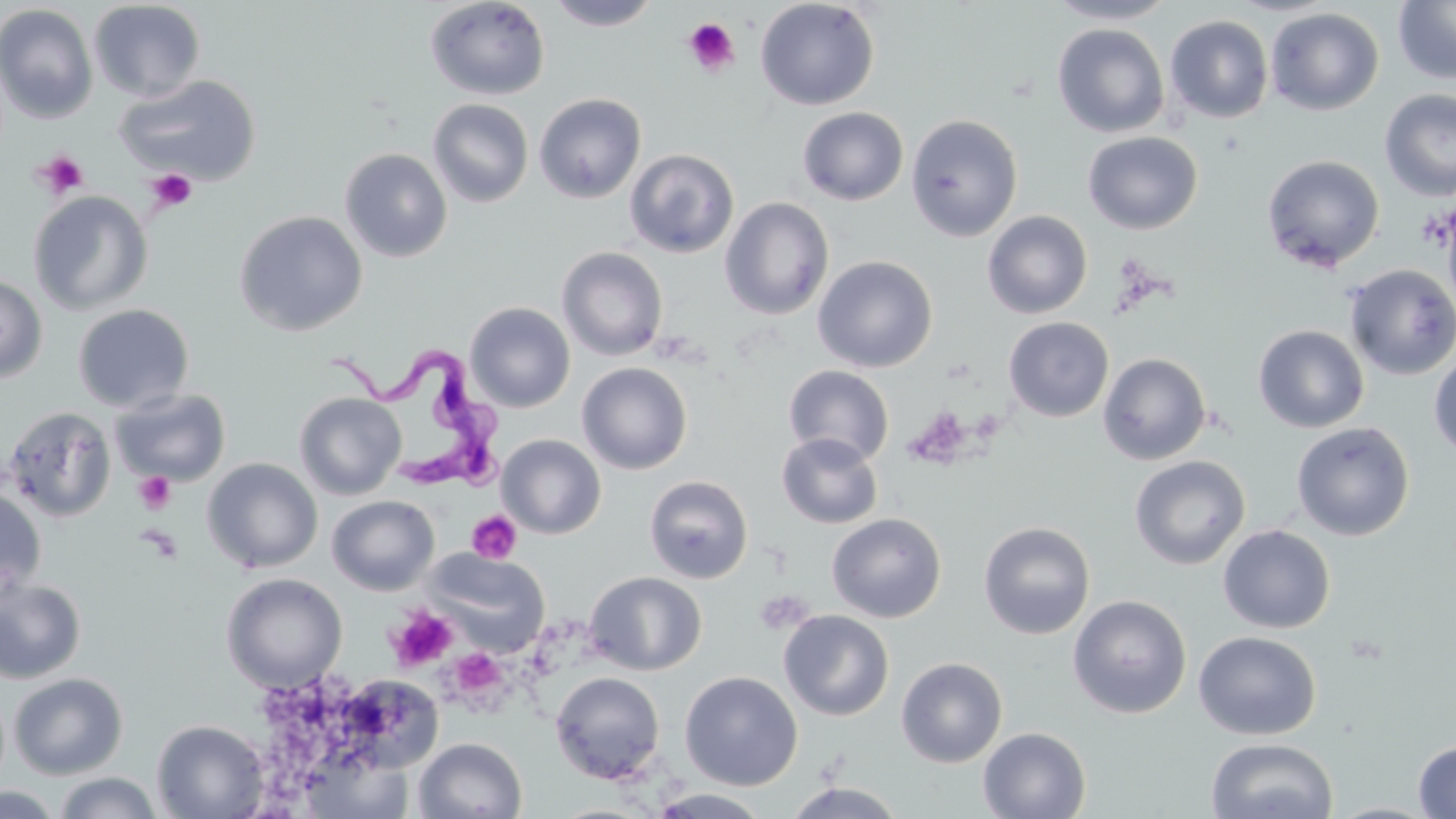

Approximate bounding boxes as [x1, y1, x2, y2] in pixels. Trypanosoma brucei locations: [324, 340, 515, 493]. Platelet locations: [682, 18, 740, 76], [34, 150, 90, 198], [147, 169, 197, 213], [133, 471, 177, 514], [467, 510, 522, 564], [754, 590, 813, 635], [386, 606, 457, 671], [447, 648, 507, 703]. Uninfected red blood cell locations: [424, 0, 551, 101], [547, 0, 662, 31], [755, 0, 880, 111], [1045, 0, 1178, 25], [1393, 0, 1456, 85], [88, 1, 206, 102], [0, 4, 98, 124], [97, 4, 234, 171], [1265, 7, 1384, 115], [1165, 15, 1273, 124], [1051, 23, 1171, 138], [116, 74, 262, 186], [1379, 89, 1456, 202], [533, 93, 647, 204], [427, 98, 534, 208], [797, 107, 909, 206], [905, 114, 1023, 242], [1082, 132, 1203, 235], [339, 148, 453, 262], [624, 148, 739, 258], [1261, 154, 1385, 271], [28, 190, 153, 316], [719, 197, 834, 319], [1442, 204, 1456, 317], [234, 210, 368, 336], [981, 210, 1093, 319], [556, 246, 668, 361], [812, 255, 938, 372], [1344, 264, 1456, 380], [0, 274, 48, 383], [464, 302, 576, 413], [73, 304, 194, 413], [1003, 317, 1114, 421], [1253, 324, 1369, 433], [1098, 352, 1212, 466], [1428, 352, 1456, 460], [576, 362, 693, 474], [783, 364, 894, 466], [110, 387, 231, 487], [295, 392, 407, 500], [2, 405, 117, 522], [1291, 422, 1415, 541], [776, 433, 883, 529], [497, 434, 606, 539], [1129, 455, 1250, 570], [202, 458, 323, 573], [644, 475, 753, 584], [0, 486, 46, 599], [327, 495, 440, 595], [826, 513, 947, 623], [978, 520, 1095, 639], [1217, 524, 1336, 634], [422, 549, 550, 655], [584, 571, 707, 675], [221, 572, 348, 693], [0, 575, 87, 684], [1067, 594, 1192, 719], [778, 610, 894, 721], [1193, 631, 1321, 740], [896, 657, 1008, 768], [680, 671, 803, 790], [8, 672, 128, 780], [550, 672, 665, 784], [338, 674, 444, 774], [151, 719, 270, 818], [978, 727, 1091, 818], [414, 737, 528, 819], [1205, 737, 1338, 819], [1413, 739, 1456, 818], [304, 749, 411, 818], [52, 772, 165, 819], [783, 782, 906, 818], [0, 786, 64, 818], [647, 788, 772, 818], [1324, 802, 1440, 819]. Slide-level diagnosis: Trypanosoma brucei. Image is 1456×819 pixels. One field of a larger specimen. Thin blood film. Optical microscopy. Captured at 1000x magnification. May-Grünwald-Giemsa-stained preparation.